Assess this cell for malaria.
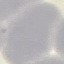
Uninfected.

Summary:
  - Stain: Giemsa
  - Capture: smartphone camera at the microscope eyepiece
  - Image type: cell patch, automatically extracted from a larger field of view and resized to 64 × 64 pixels
  - Preparation: thin blood film